Give the preparation type.
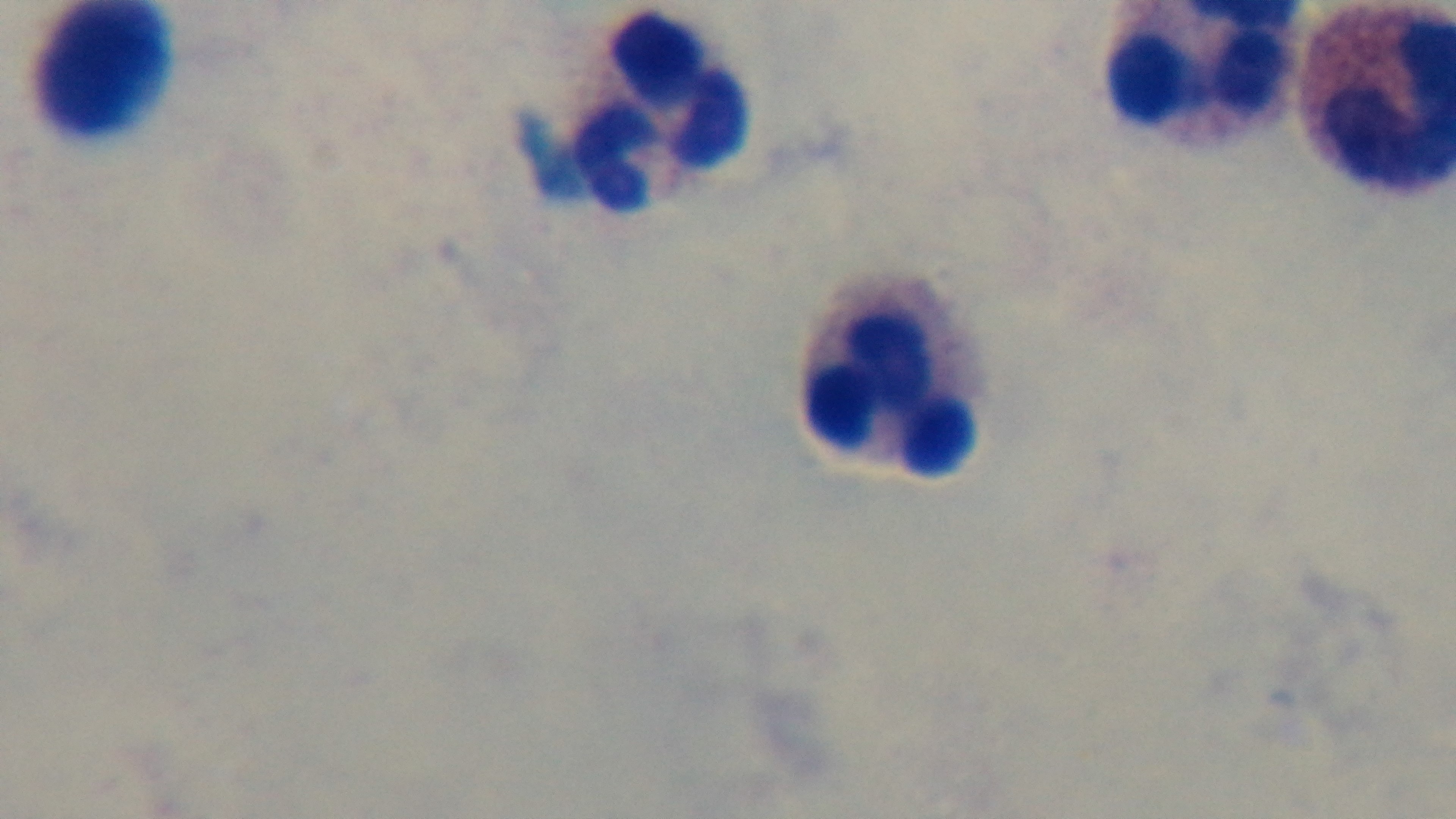

It is a thick blood film.

Summary:
  - Objective: 100x oil immersion
  - Field of view: one from the slide
  - Malaria status: uninfected
  - Modality: light microscopy
  - Stain: Giemsa
  - Capture: mounted 4K digital camera